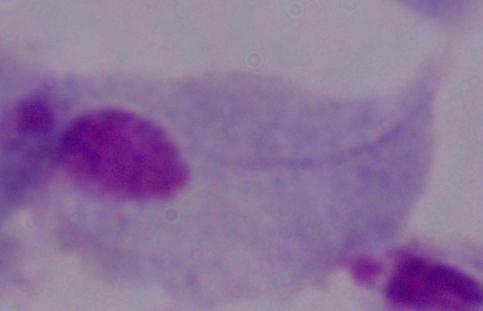

Summary:
  - Magnification: 1000x
  - Identification: trichomonad
  - Modality: micrograph